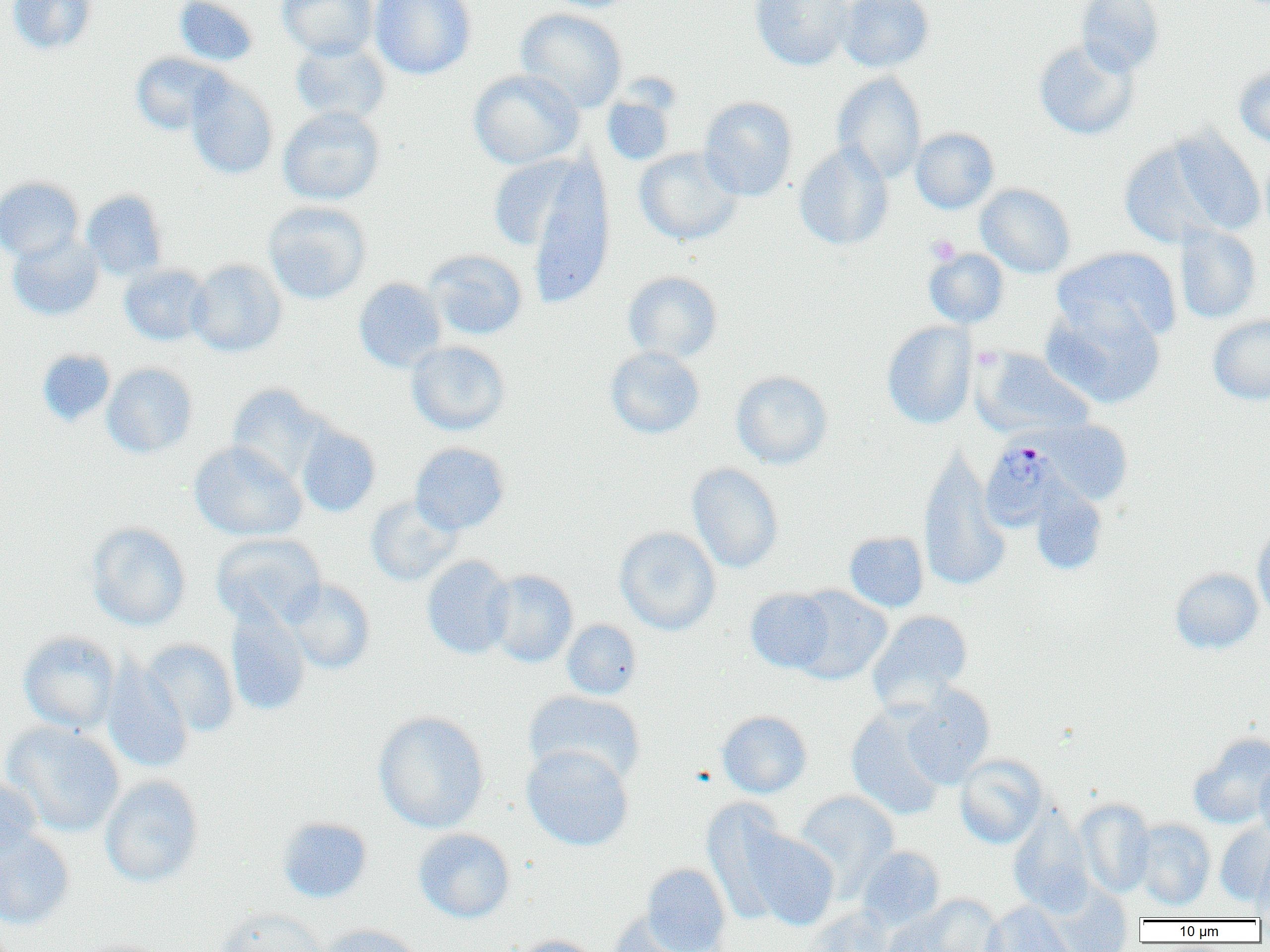

Summary:
  - Coordinate format: approximate bounding boxes as [x1, y1, x2, y2] in pixels
  - Uninfected red blood cell locations: [7, 0, 97, 55], [173, 0, 259, 67], [277, 0, 378, 60], [370, 0, 477, 79], [539, 0, 637, 13], [750, 0, 855, 71], [837, 0, 934, 72], [1075, 0, 1164, 76], [515, 8, 627, 112], [1033, 39, 1139, 140], [290, 40, 391, 125], [130, 52, 230, 135], [1234, 66, 1270, 147], [468, 69, 584, 169], [832, 72, 927, 183], [184, 74, 278, 179], [601, 93, 675, 165], [699, 96, 798, 201], [278, 106, 385, 205], [911, 128, 999, 214], [1170, 129, 1265, 236], [1118, 141, 1221, 248], [794, 142, 894, 251], [634, 147, 743, 246], [1261, 149, 1270, 244], [485, 152, 597, 257], [517, 157, 615, 306], [0, 176, 84, 263], [975, 183, 1076, 278], [82, 190, 168, 280], [263, 201, 371, 304], [1174, 224, 1262, 324], [7, 232, 103, 321], [1052, 247, 1181, 343], [924, 248, 1010, 328], [425, 249, 528, 340], [186, 259, 287, 357], [119, 264, 212, 346], [623, 271, 723, 363], [353, 278, 447, 372], [1042, 304, 1165, 408], [1208, 315, 1270, 404], [882, 321, 977, 429], [406, 340, 510, 435], [605, 346, 705, 439], [37, 349, 115, 426], [974, 349, 1093, 437], [102, 363, 198, 458], [731, 371, 833, 469], [226, 384, 329, 485], [1043, 420, 1133, 504], [296, 425, 380, 517], [189, 441, 306, 541], [411, 442, 510, 534], [918, 448, 1010, 591], [687, 463, 784, 573], [1030, 484, 1109, 575], [366, 495, 462, 586], [87, 522, 191, 631], [1252, 525, 1270, 622], [614, 526, 720, 635], [844, 531, 929, 612], [211, 533, 326, 628], [421, 555, 515, 659], [1169, 567, 1263, 654], [485, 570, 578, 667], [285, 579, 375, 674], [788, 586, 892, 684], [746, 588, 837, 673], [225, 605, 310, 716], [867, 610, 973, 709], [561, 619, 642, 700], [18, 631, 121, 734], [141, 640, 239, 736], [101, 659, 193, 773], [900, 684, 996, 788], [524, 690, 645, 787], [846, 704, 948, 820], [373, 710, 490, 834], [717, 710, 813, 798], [3, 721, 126, 838], [1189, 733, 1270, 830], [521, 744, 634, 851], [954, 754, 1049, 849], [1254, 761, 1270, 841], [0, 775, 42, 860], [99, 775, 204, 887], [794, 790, 900, 895], [1075, 798, 1156, 898], [701, 799, 793, 923], [1008, 806, 1094, 916], [277, 817, 373, 903], [1133, 819, 1215, 910], [1215, 824, 1270, 905], [0, 827, 75, 930], [413, 828, 515, 923], [745, 829, 840, 930], [857, 846, 945, 930], [1251, 846, 1270, 920], [642, 863, 731, 952], [1047, 885, 1133, 952], [911, 894, 1006, 952], [982, 901, 1076, 952], [806, 906, 895, 952], [215, 907, 327, 952], [608, 913, 700, 952], [879, 913, 961, 952], [317, 924, 423, 952], [509, 935, 603, 952], [71, 937, 170, 952]
  - Plasmodium malariae-infected red blood cell locations: [982, 436, 1056, 533]
  - Platelet locations: [926, 235, 960, 264]
  - Slide-level diagnosis: Plasmodium malariae
  - Modality: optical microscopy
  - Field of view: single
  - Image size: 1270×952 pixels
  - Preparation: thin blood smear
  - Magnification: 1000x